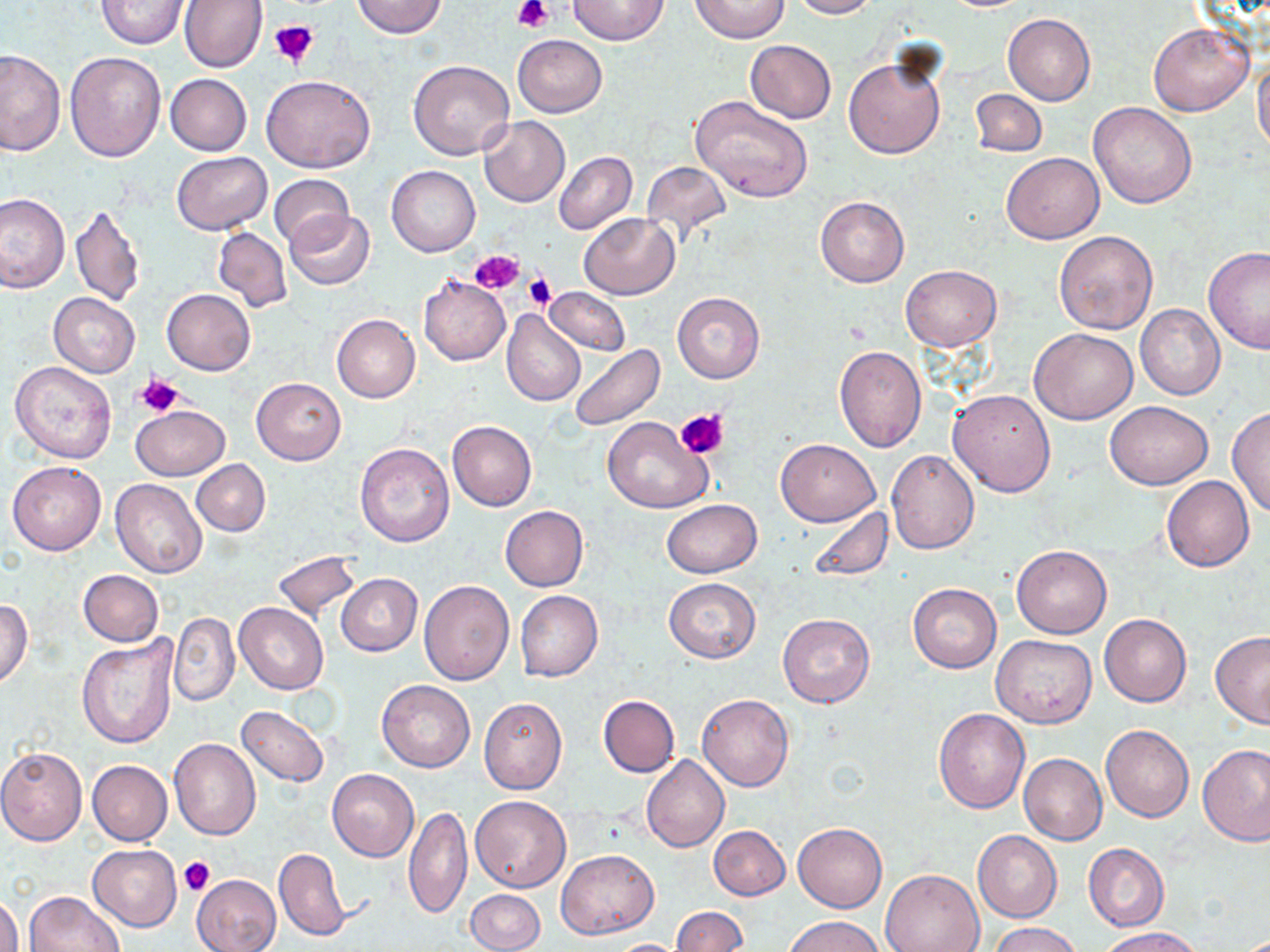

Approximate bounding boxes as named x1/y1/x2/y2 corners in pixels. Uninfected red blood cell locations: (x1=180, y1=0, x2=267, y2=73), (x1=350, y1=0, x2=448, y2=39), (x1=567, y1=0, x2=667, y2=45), (x1=691, y1=0, x2=788, y2=43), (x1=787, y1=0, x2=878, y2=19), (x1=96, y1=1, x2=189, y2=49), (x1=1003, y1=14, x2=1096, y2=105), (x1=1148, y1=20, x2=1254, y2=116), (x1=512, y1=35, x2=606, y2=117), (x1=745, y1=41, x2=836, y2=123), (x1=1, y1=49, x2=67, y2=156), (x1=842, y1=51, x2=947, y2=159), (x1=65, y1=52, x2=166, y2=161), (x1=408, y1=58, x2=515, y2=160), (x1=1253, y1=60, x2=1270, y2=155), (x1=165, y1=74, x2=251, y2=155), (x1=261, y1=74, x2=376, y2=173), (x1=970, y1=89, x2=1047, y2=156), (x1=691, y1=96, x2=812, y2=202), (x1=1089, y1=101, x2=1198, y2=209), (x1=479, y1=116, x2=570, y2=207), (x1=554, y1=151, x2=637, y2=235), (x1=1001, y1=151, x2=1104, y2=244), (x1=172, y1=152, x2=272, y2=234), (x1=641, y1=162, x2=732, y2=237), (x1=386, y1=166, x2=479, y2=256), (x1=268, y1=173, x2=355, y2=249), (x1=0, y1=193, x2=68, y2=293), (x1=815, y1=196, x2=908, y2=287), (x1=70, y1=204, x2=145, y2=306), (x1=283, y1=210, x2=376, y2=290), (x1=578, y1=213, x2=681, y2=299), (x1=213, y1=227, x2=291, y2=312), (x1=1053, y1=230, x2=1158, y2=334), (x1=1203, y1=246, x2=1270, y2=352), (x1=900, y1=265, x2=1001, y2=351), (x1=419, y1=275, x2=510, y2=365), (x1=545, y1=286, x2=629, y2=357), (x1=162, y1=289, x2=255, y2=375), (x1=672, y1=292, x2=764, y2=384), (x1=48, y1=294, x2=139, y2=378), (x1=1135, y1=304, x2=1225, y2=402), (x1=502, y1=311, x2=586, y2=406), (x1=331, y1=314, x2=420, y2=402), (x1=1030, y1=328, x2=1138, y2=425), (x1=567, y1=343, x2=664, y2=431), (x1=834, y1=345, x2=928, y2=452), (x1=11, y1=360, x2=119, y2=464), (x1=252, y1=377, x2=345, y2=465), (x1=948, y1=389, x2=1057, y2=497), (x1=1105, y1=400, x2=1213, y2=488), (x1=131, y1=404, x2=229, y2=480), (x1=1228, y1=407, x2=1270, y2=519), (x1=604, y1=416, x2=712, y2=513), (x1=447, y1=421, x2=537, y2=511), (x1=775, y1=438, x2=882, y2=526), (x1=355, y1=443, x2=455, y2=547), (x1=886, y1=450, x2=979, y2=555), (x1=192, y1=459, x2=270, y2=535), (x1=8, y1=461, x2=106, y2=555), (x1=1161, y1=476, x2=1255, y2=572), (x1=111, y1=479, x2=208, y2=578), (x1=662, y1=500, x2=762, y2=577), (x1=806, y1=505, x2=894, y2=585), (x1=500, y1=506, x2=588, y2=591), (x1=1011, y1=545, x2=1112, y2=638), (x1=274, y1=551, x2=361, y2=621), (x1=77, y1=569, x2=164, y2=647), (x1=336, y1=573, x2=421, y2=656), (x1=664, y1=578, x2=760, y2=662), (x1=419, y1=579, x2=515, y2=685), (x1=908, y1=584, x2=1002, y2=672), (x1=515, y1=590, x2=603, y2=681), (x1=0, y1=599, x2=33, y2=687), (x1=234, y1=602, x2=328, y2=695), (x1=169, y1=612, x2=239, y2=707), (x1=778, y1=614, x2=875, y2=708), (x1=1099, y1=614, x2=1192, y2=707), (x1=1210, y1=630, x2=1270, y2=728), (x1=77, y1=634, x2=178, y2=749), (x1=991, y1=634, x2=1096, y2=727), (x1=376, y1=680, x2=475, y2=772), (x1=598, y1=694, x2=680, y2=777), (x1=696, y1=694, x2=795, y2=791), (x1=478, y1=697, x2=567, y2=795), (x1=237, y1=705, x2=329, y2=787), (x1=933, y1=708, x2=1030, y2=812), (x1=1100, y1=724, x2=1194, y2=822), (x1=169, y1=738, x2=261, y2=841), (x1=0, y1=746, x2=87, y2=846), (x1=1199, y1=746, x2=1270, y2=848), (x1=1018, y1=753, x2=1108, y2=844), (x1=642, y1=755, x2=730, y2=852), (x1=87, y1=760, x2=172, y2=846), (x1=328, y1=769, x2=418, y2=861), (x1=469, y1=796, x2=572, y2=893), (x1=404, y1=802, x2=471, y2=922), (x1=792, y1=822, x2=887, y2=912), (x1=709, y1=825, x2=790, y2=900), (x1=973, y1=830, x2=1063, y2=922), (x1=87, y1=844, x2=182, y2=931), (x1=1083, y1=844, x2=1169, y2=931), (x1=273, y1=847, x2=350, y2=942), (x1=556, y1=848, x2=660, y2=939), (x1=881, y1=869, x2=984, y2=952), (x1=191, y1=874, x2=282, y2=952), (x1=24, y1=890, x2=125, y2=952), (x1=466, y1=890, x2=545, y2=952), (x1=1, y1=893, x2=22, y2=952), (x1=671, y1=907, x2=747, y2=952), (x1=783, y1=914, x2=886, y2=952), (x1=990, y1=922, x2=1083, y2=952), (x1=1098, y1=927, x2=1204, y2=952), (x1=604, y1=939, x2=691, y2=951). Platelet locations: (x1=513, y1=0, x2=553, y2=32), (x1=269, y1=17, x2=320, y2=67), (x1=468, y1=250, x2=524, y2=294), (x1=525, y1=271, x2=555, y2=311), (x1=136, y1=371, x2=185, y2=417), (x1=675, y1=407, x2=728, y2=461), (x1=177, y1=856, x2=215, y2=897). Slide-level diagnosis: negative for blood parasites. Single field of view. May-Grünwald-Giemsa-stained preparation. Light microscopy. Thin blood film. Image is 1270×952 pixels. 1000x magnification.